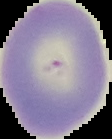

Result: no Plasmodium parasites detected. From a thin blood film. Image is 112×139 pixels. Segmented cell region on a black background.